Name the parasite shown.
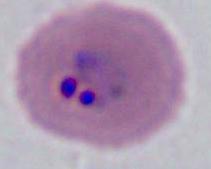
This is Plasmodium.

Summary:
  - Magnification: 400x or 1000x
  - Modality: photomicrograph